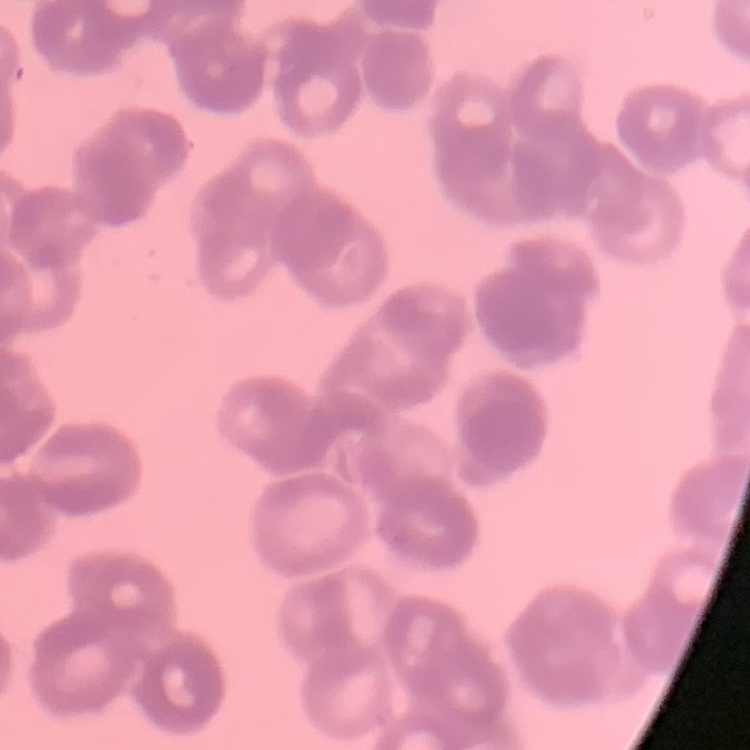
{
  "red_blood_cell_morphology": "rouleaux formation",
  "stain": "Field's or Giemsa",
  "preparation": "thin blood film",
  "image_type": "one tile cut from a larger photomicrograph"
}